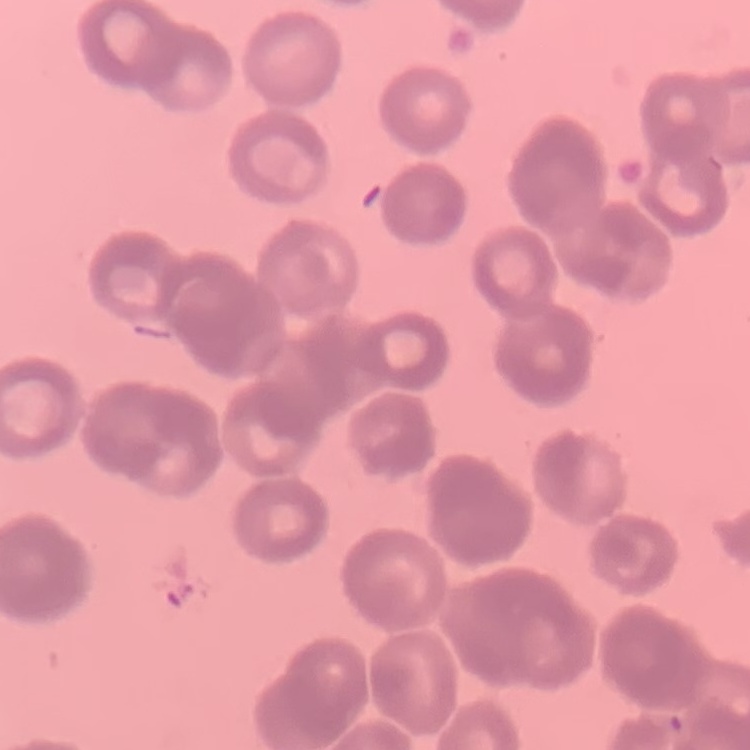

Summary:
  - Erythrocyte morphology: rouleaux formation
  - Preparation: thin blood film
  - Image type: one tile cut from a larger photomicrograph
  - Stain: Field's or Giemsa